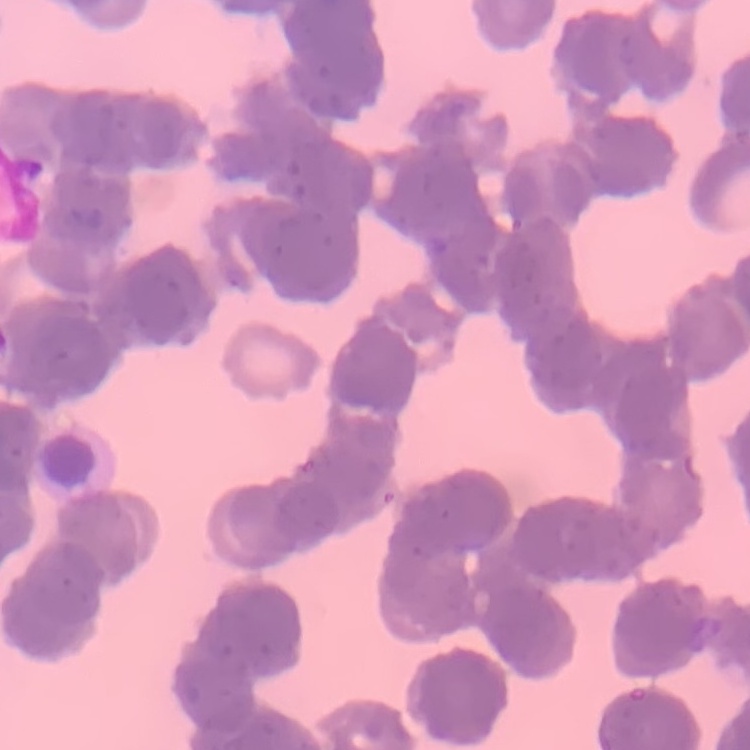

The erythrocytes show rouleaux formation. Field's or Giemsa stain. Square crop of a larger photomicrograph. Thin blood smear.